Give the position of every Plasmodium parasite.
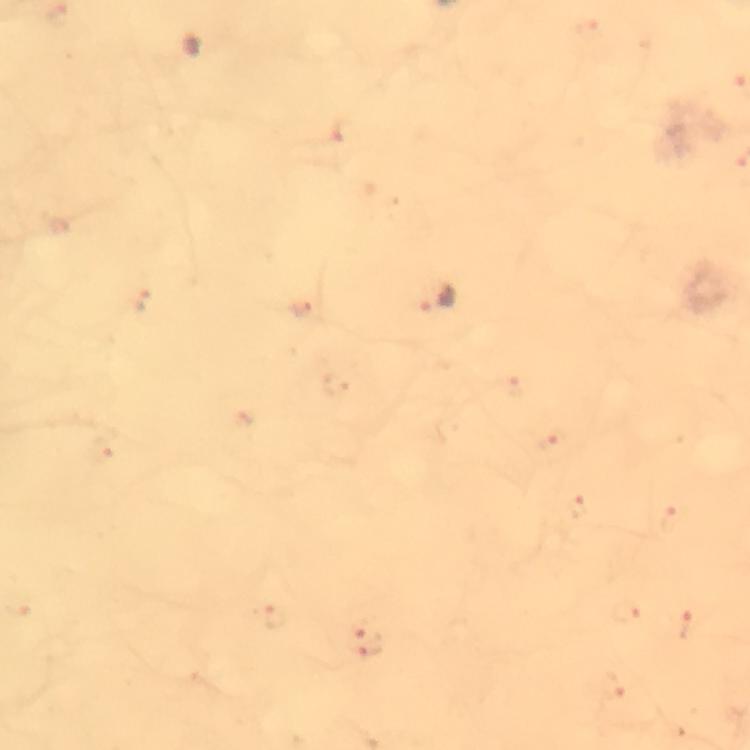
Approximate centers as {x, y} in pixels.
Plasmodium parasites: {439, 300}.

magnification = 100x
cropped from = one field of view
preparation = thick blood film
capture = smartphone mounted on the microscope
stain = Giemsa
image size = 750×750 pixels
context = from a diagnostic examination for malaria
immersion oil = used